Assess this cell for malaria.
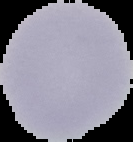
It is uninfected.

{
  "image_type": "segmented cell region on a black background",
  "preparation": "thin blood film",
  "image_size": "133×142 pixels"
}